Comment on the morphology of the erythrocytes.
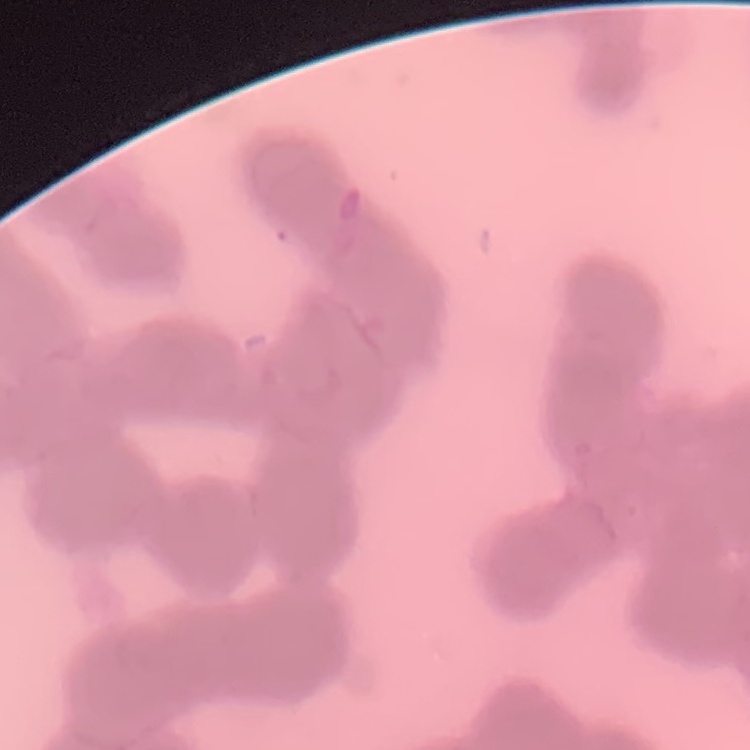
Rouleaux formation.

{
  "preparation": "thin blood smear",
  "stain": "Field's or Giemsa",
  "image_type": "square crop of a larger photomicrograph"
}